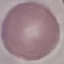 Malaria status: uninfected. Cell patch, automatically extracted from a larger field of view and resized to 64 × 64 pixels. Thin blood smear. Giemsa-stained preparation. Photographed with a smartphone camera at the microscope eyepiece.